Outline platelets.
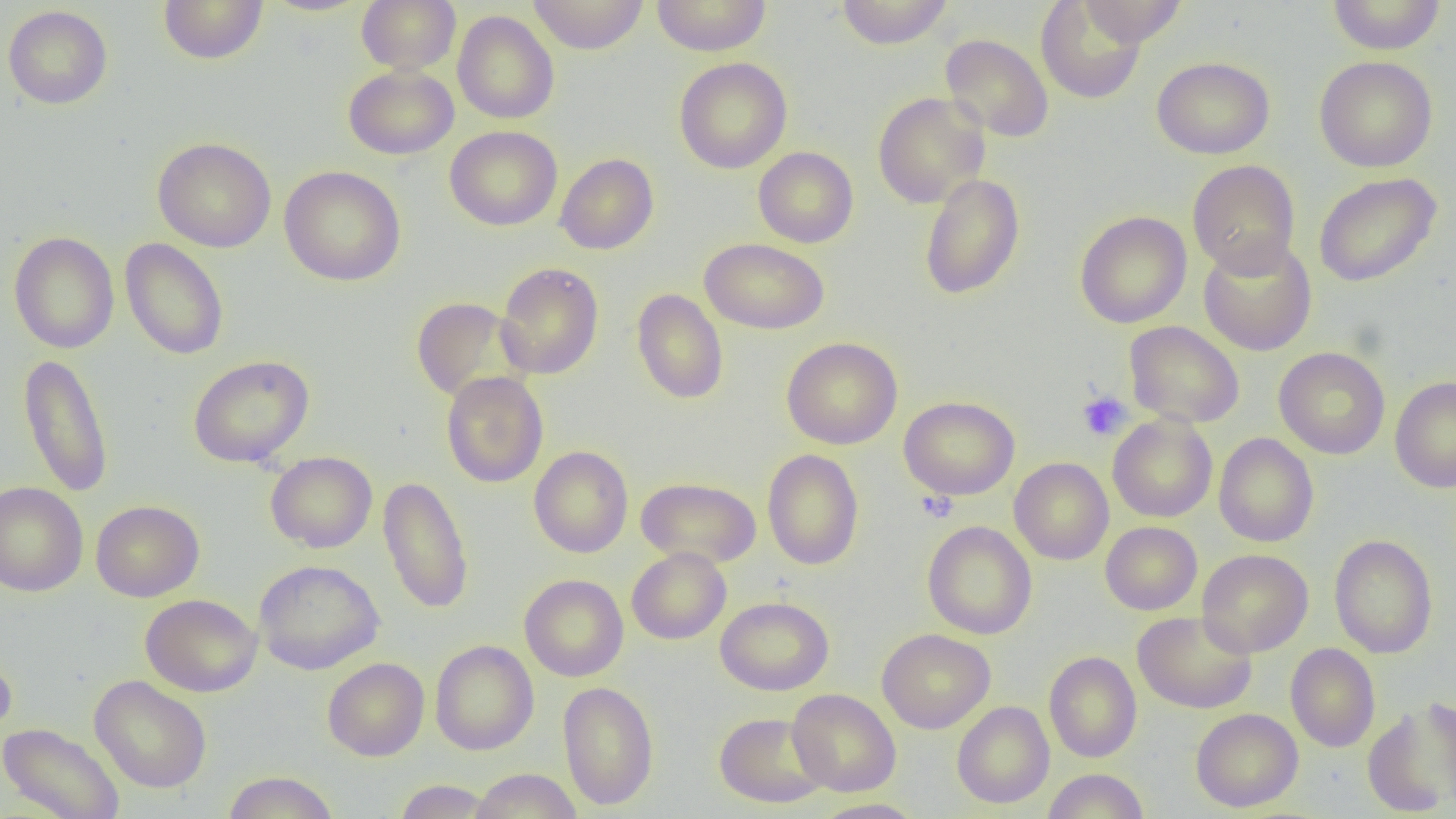

Approximate bounding boxes as (x1,y1)-(x2,y2) corner pairs in pixels.
Platelets: (1077,390)-(1132,441), (917,491)-(957,522).

slide-level diagnosis = no evidence of blood parasites
image size = 1456×819 pixels
uninfected red blood cell locations = approximate bounding boxes as (x1,y1)-(x2,y2) corner pairs in pixels: (158,0)-(269,65), (259,0)-(374,17), (357,0)-(461,73), (528,0)-(649,54), (651,0)-(771,56), (836,0)-(954,49), (1079,0)-(1187,47), (1327,0)-(1446,55), (1036,1)-(1146,105), (3,5)-(113,109), (453,11)-(559,124), (940,34)-(1054,142), (1151,56)-(1275,159), (1314,56)-(1438,172), (674,57)-(792,174), (343,65)-(459,159), (872,91)-(990,208), (444,126)-(563,231), (152,137)-(276,252), (753,146)-(858,248), (555,153)-(659,254), (1188,160)-(1300,276), (279,166)-(406,287), (1314,172)-(1442,287), (919,173)-(1025,300), (1074,211)-(1191,328), (8,231)-(120,354), (699,237)-(829,334), (1198,237)-(1317,356), (120,238)-(229,360), (495,262)-(604,380), (631,288)-(728,404), (411,296)-(526,403), (1124,321)-(1245,428), (781,337)-(902,449), (1274,346)-(1390,459), (18,352)-(113,498), (188,354)-(314,468), (441,371)-(548,488), (1390,376)-(1456,493), (899,396)-(1020,499), (1108,414)-(1218,522), (1214,433)-(1319,547), (529,446)-(633,557), (762,449)-(864,571), (265,451)-(377,553), (1009,458)-(1114,565), (378,475)-(474,615), (636,476)-(762,568), (0,481)-(88,596), (91,499)-(204,602), (922,520)-(1037,639), (1100,521)-(1202,615), (1329,534)-(1438,658), (627,547)-(731,644), (1197,549)-(1313,657), (253,559)-(384,675), (519,574)-(628,682), (140,593)-(262,697), (715,596)-(833,695), (1133,611)-(1257,713), (877,628)-(995,734), (430,640)-(539,755), (1286,643)-(1380,751), (0,644)-(17,743), (1044,651)-(1142,762), (322,657)-(429,761), (89,674)-(212,794), (558,681)-(659,810), (787,688)-(901,796), (1362,700)-(1456,817), (952,701)-(1054,808), (1190,708)-(1303,811), (714,712)-(830,808), (0,722)-(125,819), (469,768)-(582,819), (1042,768)-(1148,819), (222,771)-(339,819), (393,779)-(497,818), (810,798)-(925,819)
modality = light microscopy
preparation = thin blood film
magnification = 1000x
field of view = single